Mark where platelets are.
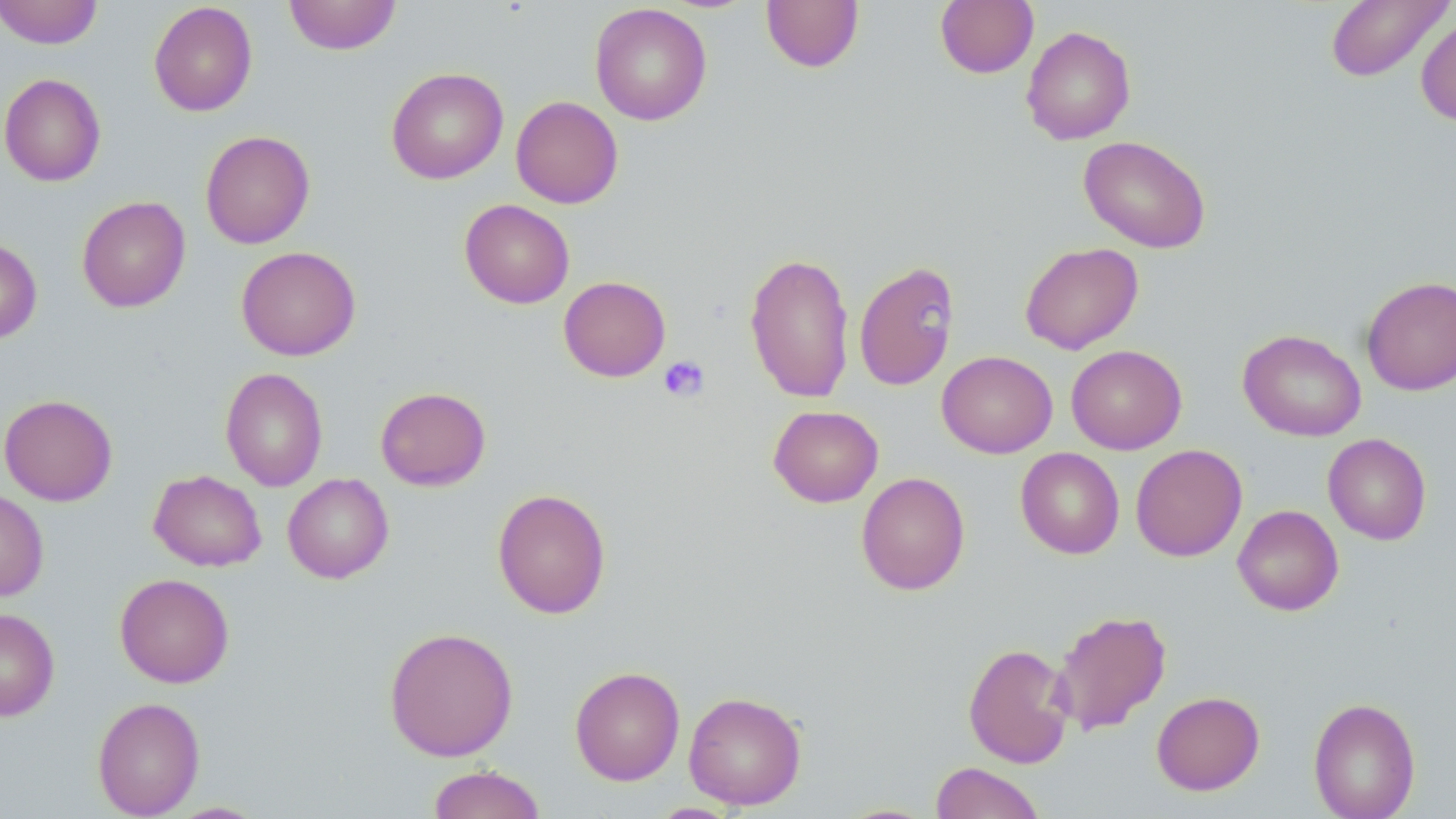
Approximate bounding boxes as [x1, y1, x2, y2] in pixels.
Platelets: [658, 355, 710, 403].

Uninfected red blood cell locations: [0, 0, 103, 49], [284, 0, 401, 55], [760, 0, 864, 73], [1325, 0, 1453, 82], [935, 1, 1038, 78], [148, 2, 258, 116], [589, 3, 712, 126], [1415, 15, 1456, 126], [1021, 25, 1136, 145], [386, 67, 508, 185], [0, 73, 106, 187], [511, 96, 623, 208], [200, 130, 315, 249], [1078, 136, 1211, 253], [77, 195, 191, 313], [459, 199, 574, 308], [0, 238, 42, 344], [1019, 242, 1144, 354], [236, 246, 361, 361], [744, 252, 855, 403], [854, 260, 959, 391], [558, 276, 671, 381], [1361, 276, 1456, 395], [1237, 329, 1366, 442], [1066, 345, 1186, 454], [937, 351, 1058, 458], [220, 367, 328, 491], [375, 386, 491, 491], [0, 394, 118, 506], [769, 405, 884, 507], [1323, 433, 1432, 545], [1130, 444, 1247, 562], [1015, 447, 1125, 559], [148, 470, 267, 571], [856, 472, 971, 595], [282, 473, 394, 583], [492, 488, 612, 619], [0, 489, 49, 601], [1233, 504, 1344, 616], [115, 573, 234, 688], [0, 607, 59, 722], [1050, 609, 1172, 736], [384, 626, 519, 761], [962, 643, 1074, 769], [569, 666, 685, 786], [683, 690, 807, 810], [1151, 691, 1265, 795], [92, 697, 205, 818], [1307, 697, 1421, 819], [929, 762, 1046, 819], [427, 764, 546, 819], [645, 802, 745, 818], [831, 802, 943, 818]. Slide-level diagnosis: no evidence of blood parasites. 1000x magnification. Image is 1456×819 pixels. Thin blood smear. One field of a larger specimen. May-Grünwald-Giemsa-stained preparation. Optical microscopy.